Locate every uninfected red blood cell.
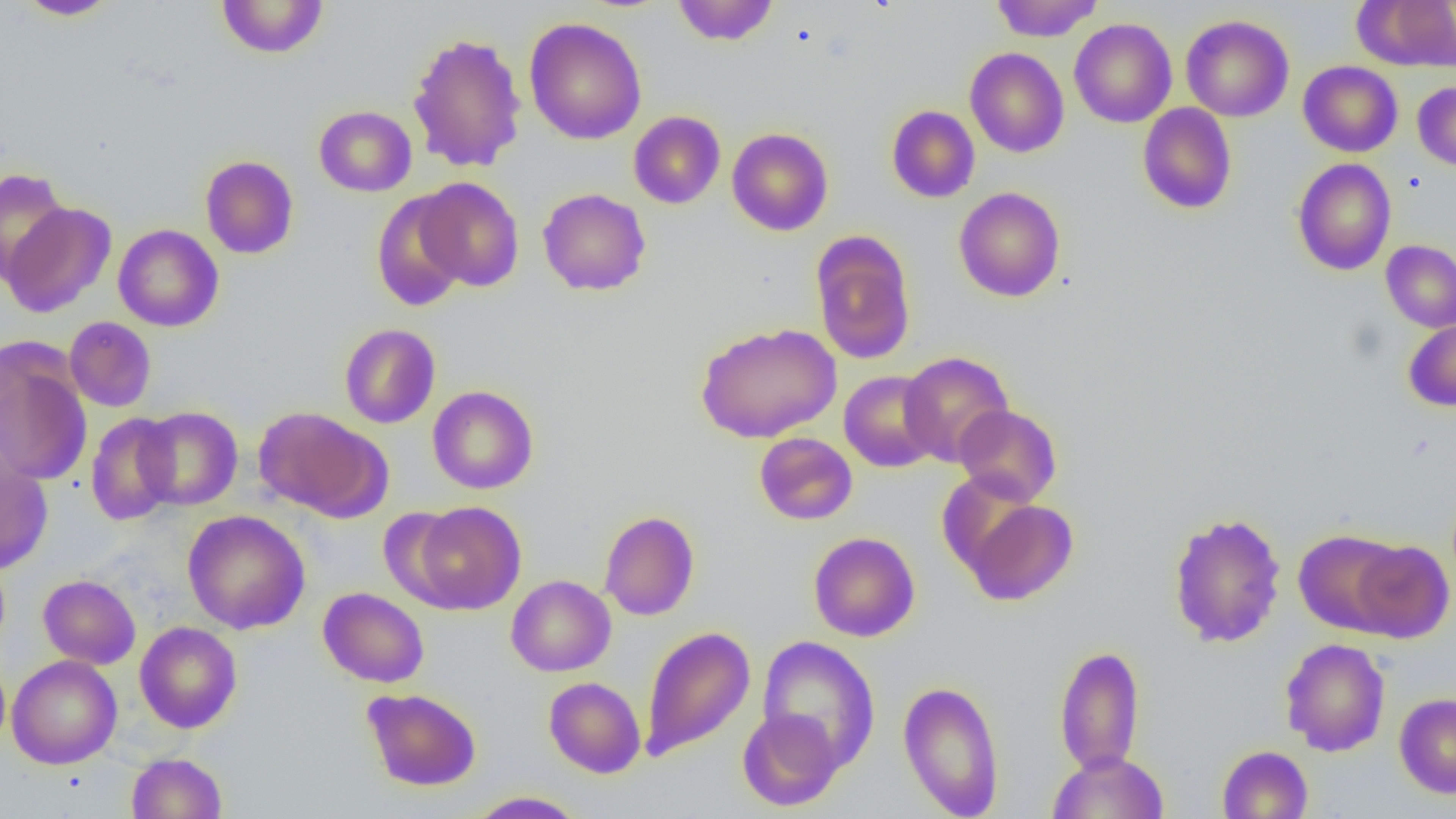

Approximate bounding boxes as (x1,y1)-(x2,y2) corner pairs in pixels.
Uninfected red blood cells: (14,0)-(119,20), (215,0)-(329,59), (672,0)-(779,46), (990,0)-(1102,42), (1354,0)-(1455,72), (1180,15)-(1294,122), (524,17)-(647,145), (1069,18)-(1177,128), (407,32)-(527,173), (965,48)-(1069,158), (1298,61)-(1403,157), (1412,82)-(1456,171), (1137,103)-(1237,214), (886,105)-(980,203), (314,106)-(416,197), (628,111)-(726,209), (727,127)-(833,236), (200,155)-(299,259), (1292,158)-(1397,275), (0,168)-(71,285), (415,176)-(525,292), (954,187)-(1066,302), (538,188)-(651,296), (370,191)-(468,312), (2,202)-(116,318), (113,224)-(224,332), (811,230)-(916,366), (1381,240)-(1456,333), (64,316)-(157,412), (1404,318)-(1456,411), (339,323)-(440,428), (695,323)-(841,443), (898,351)-(1014,466), (0,353)-(93,486), (839,370)-(942,473), (427,385)-(539,494), (953,404)-(1062,506), (136,406)-(243,510), (255,407)-(386,519), (85,412)-(180,526), (753,432)-(858,525), (0,460)-(53,574), (958,496)-(1079,606), (408,501)-(526,614), (182,509)-(310,634), (1167,510)-(1287,649), (599,511)-(699,621), (1293,528)-(1408,635), (808,531)-(921,642), (1347,539)-(1455,642), (38,575)-(141,669), (506,575)-(616,677), (317,587)-(429,688), (135,621)-(242,734), (640,625)-(756,762), (757,636)-(880,771), (1280,638)-(1391,757), (1054,645)-(1145,774), (0,653)-(10,752), (7,654)-(122,769), (543,676)-(646,778), (898,679)-(1005,818), (361,688)-(482,792), (1394,692)-(1456,798), (737,709)-(844,811), (1217,744)-(1313,818), (1048,751)-(1169,818), (126,753)-(227,818), (467,791)-(587,818).

Slide-level diagnosis: no evidence of blood parasites. Thin blood smear. Optical microscopy. Image is 1456×819 pixels. 1000x magnification. Single field of view.